Give the position of every Plasmodium parasite.
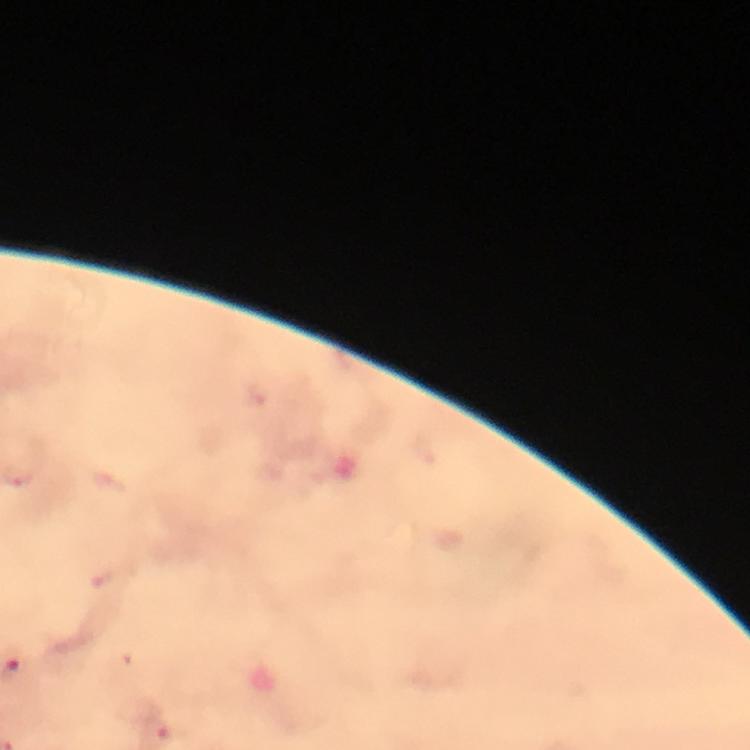

Approximate centers as {x, y} in pixels.
Plasmodium parasites: {20, 476}, {156, 731}.

cropped from = one field of view
capture = smartphone camera through the microscope
image size = 750×750 pixels
context = from a malaria diagnostic workup
immersion oil = applied
preparation = thick smear
stain = Giemsa
magnification = 100x